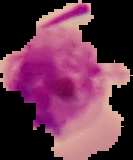 Result: Plasmodium parasites detected. From a thin blood smear. The area outside the segmented cell region is set to black. Image is 133×160 pixels.